Locate every blood parasite and identify its species.
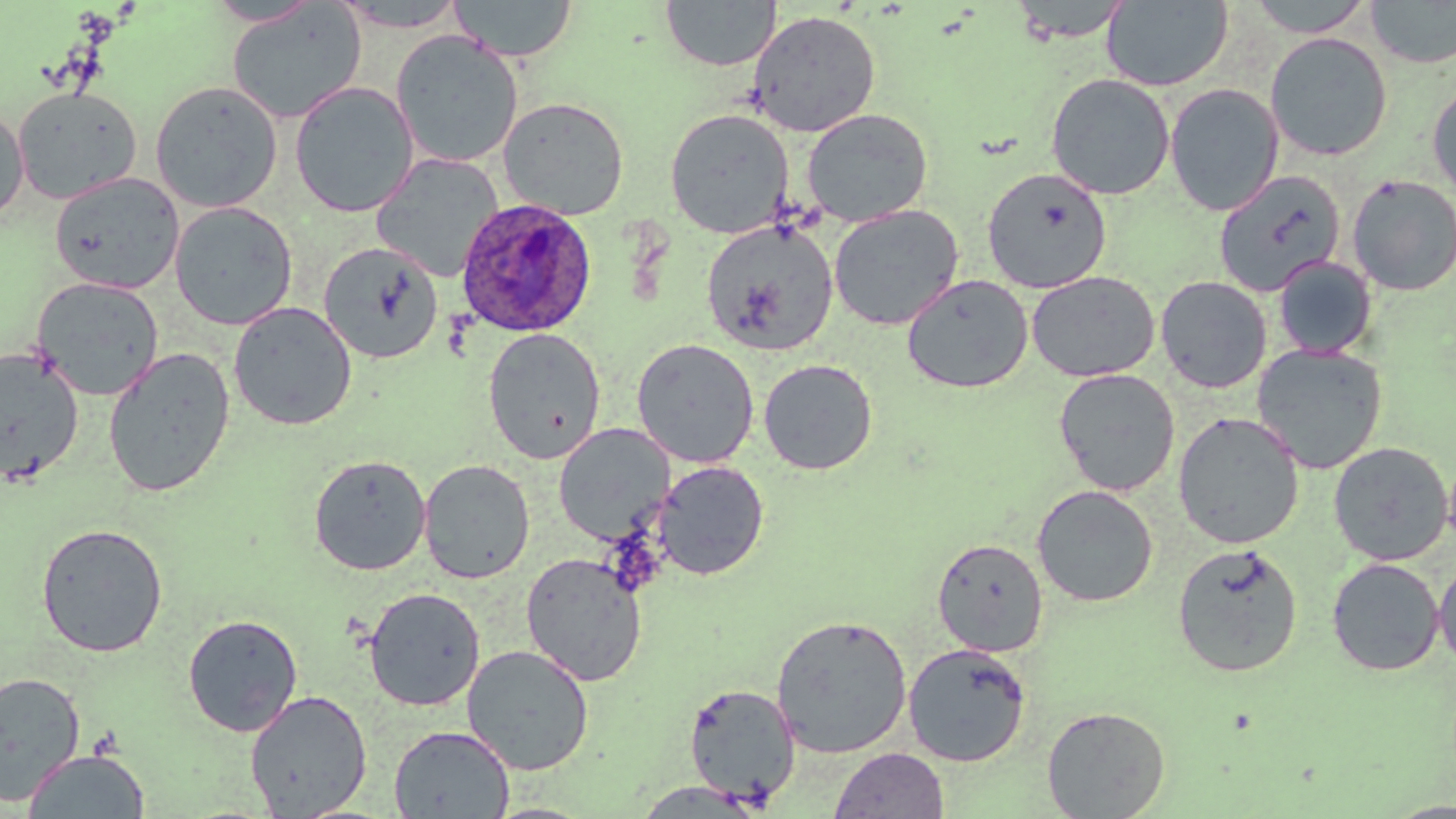

Approximate bounding boxes as [x1, y1, x2, y2] in pixels.
Plasmodium ovale-infected red blood cells: [456, 198, 597, 338].
No Plasmodium falciparum, Plasmodium malariae, Plasmodium vivax, Babesia divergens, or Trypanosoma brucei observed.

slide_level_diagnosis: Plasmodium ovale
field_of_view: one of a larger specimen
uninfected_red_blood_cell_locations: 'approximate bounding boxes as [x1, y1, x2, y2] in pixels: [450, 0, 578, 62], [659, 0, 782, 71], [1007, 0, 1134, 43], [1102, 0, 1233, 91], [1247, 0, 1374, 38], [1366, 0, 1456, 68], [205, 1, 322, 27], [327, 1, 472, 32], [226, 3, 366, 124], [747, 10, 882, 137], [390, 30, 523, 168], [1265, 32, 1393, 161], [1045, 73, 1175, 200], [150, 80, 283, 213], [1427, 80, 1456, 202], [289, 81, 418, 218], [1164, 83, 1284, 216], [12, 86, 142, 205], [497, 96, 630, 220], [0, 105, 29, 224], [664, 108, 794, 238], [802, 108, 934, 227], [370, 153, 504, 281], [982, 167, 1111, 293], [1213, 169, 1347, 297], [49, 172, 185, 294], [1347, 174, 1456, 296], [169, 201, 298, 331], [828, 204, 964, 330], [700, 219, 839, 356], [319, 241, 443, 363], [1272, 255, 1379, 360], [1026, 270, 1160, 382], [901, 273, 1033, 394], [1155, 276, 1272, 394], [30, 277, 165, 401], [228, 301, 357, 430], [483, 328, 606, 464], [631, 338, 759, 467], [1252, 342, 1388, 475], [0, 347, 84, 485], [102, 347, 236, 497], [758, 358, 878, 475], [1053, 368, 1180, 496], [1173, 411, 1305, 548], [553, 424, 675, 544], [1328, 442, 1453, 566], [309, 454, 432, 576], [419, 459, 534, 584], [653, 460, 769, 581], [1031, 484, 1158, 607], [36, 522, 168, 657], [932, 537, 1049, 657], [1171, 542, 1303, 677], [521, 552, 648, 686], [1434, 554, 1456, 671], [1326, 557, 1445, 676], [363, 587, 486, 711], [183, 613, 303, 737], [770, 613, 913, 758], [903, 643, 1031, 767], [462, 644, 594, 775], [0, 671, 85, 803], [683, 682, 801, 806], [244, 690, 372, 818], [1042, 705, 1171, 818], [388, 725, 514, 818], [829, 747, 949, 818], [23, 749, 149, 818], [629, 781, 769, 816]'
modality: optical microscopy
image_size: 1456×819 pixels
preparation: thin blood smear
magnification: 1000x
stain: May-Grünwald-Giemsa